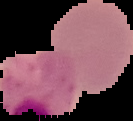
Summary:
  - Malaria status: uninfected
  - Image size: 133×121 pixels
  - Preparation: thin blood film
  - Image type: cell region segmented out of the field of view; surrounding area masked to black